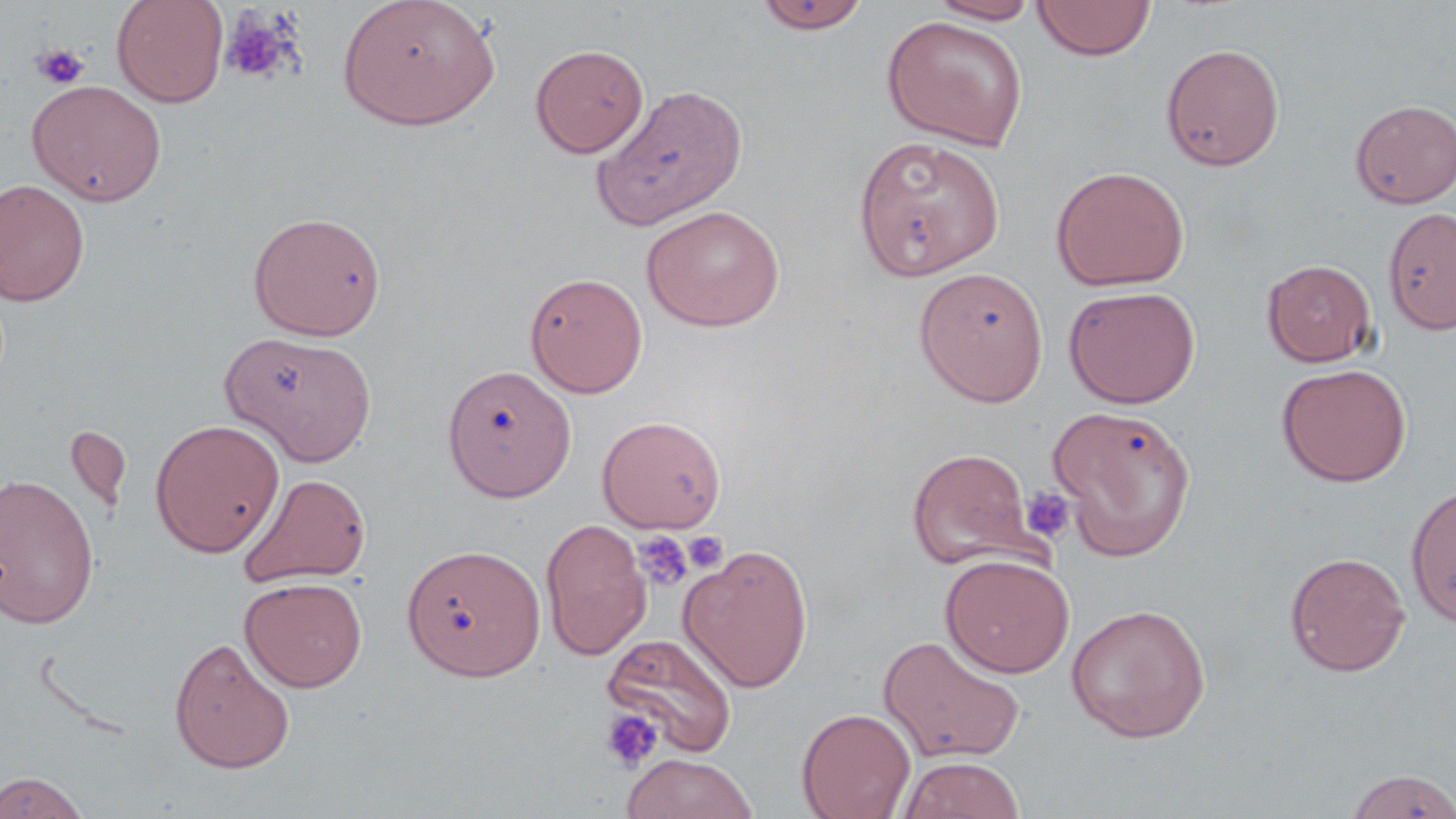 Approximate bounding boxes as (x1, y1, x2, y2) in pixels. Uninfected red blood cell locations: (111, 0, 229, 108), (337, 0, 500, 130), (927, 0, 1042, 24), (1032, 0, 1157, 61), (753, 1, 872, 34), (881, 14, 1029, 151), (1160, 42, 1285, 171), (530, 44, 649, 158), (27, 80, 166, 206), (591, 83, 748, 229), (1350, 99, 1456, 209), (853, 136, 1004, 281), (1051, 166, 1190, 291), (0, 178, 90, 306), (641, 204, 785, 331), (1383, 206, 1456, 335), (247, 210, 387, 341), (1262, 259, 1377, 367), (913, 266, 1049, 407), (524, 272, 648, 398), (1063, 285, 1201, 408), (220, 330, 378, 466), (1275, 362, 1412, 487), (442, 364, 577, 502), (1047, 404, 1197, 561), (597, 415, 726, 533), (149, 418, 285, 558), (65, 425, 132, 515), (907, 447, 1040, 572), (237, 472, 370, 588), (0, 473, 99, 629), (1404, 483, 1456, 630), (540, 518, 652, 660), (678, 542, 814, 693), (402, 543, 545, 680), (1284, 551, 1411, 676), (940, 553, 1075, 678), (240, 576, 367, 692), (1066, 603, 1211, 743), (601, 632, 738, 759), (877, 633, 1026, 764), (169, 636, 296, 773), (797, 707, 916, 819), (621, 753, 758, 819), (897, 756, 1026, 819), (1344, 768, 1456, 818), (0, 771, 89, 818). Platelet locations: (220, 6, 302, 86), (31, 43, 90, 89), (1021, 487, 1076, 544), (632, 530, 694, 592), (683, 530, 728, 573), (599, 707, 663, 773). Slide-level diagnosis: negative for blood parasites. Single field of view. Captured at 1000x magnification. Light microscopy. May-Grünwald-Giemsa-stained preparation. Thin blood smear. Image is 1456×819 pixels.